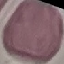

Summary:
  - Result: no malaria parasites seen
  - Capture: smartphone camera at the microscope eyepiece
  - Preparation: thin blood smear
  - Stain: Giemsa
  - Image type: automatically extracted cell patch, resized to 64 × 64 pixels